Evaluate for parasitized red blood cells.
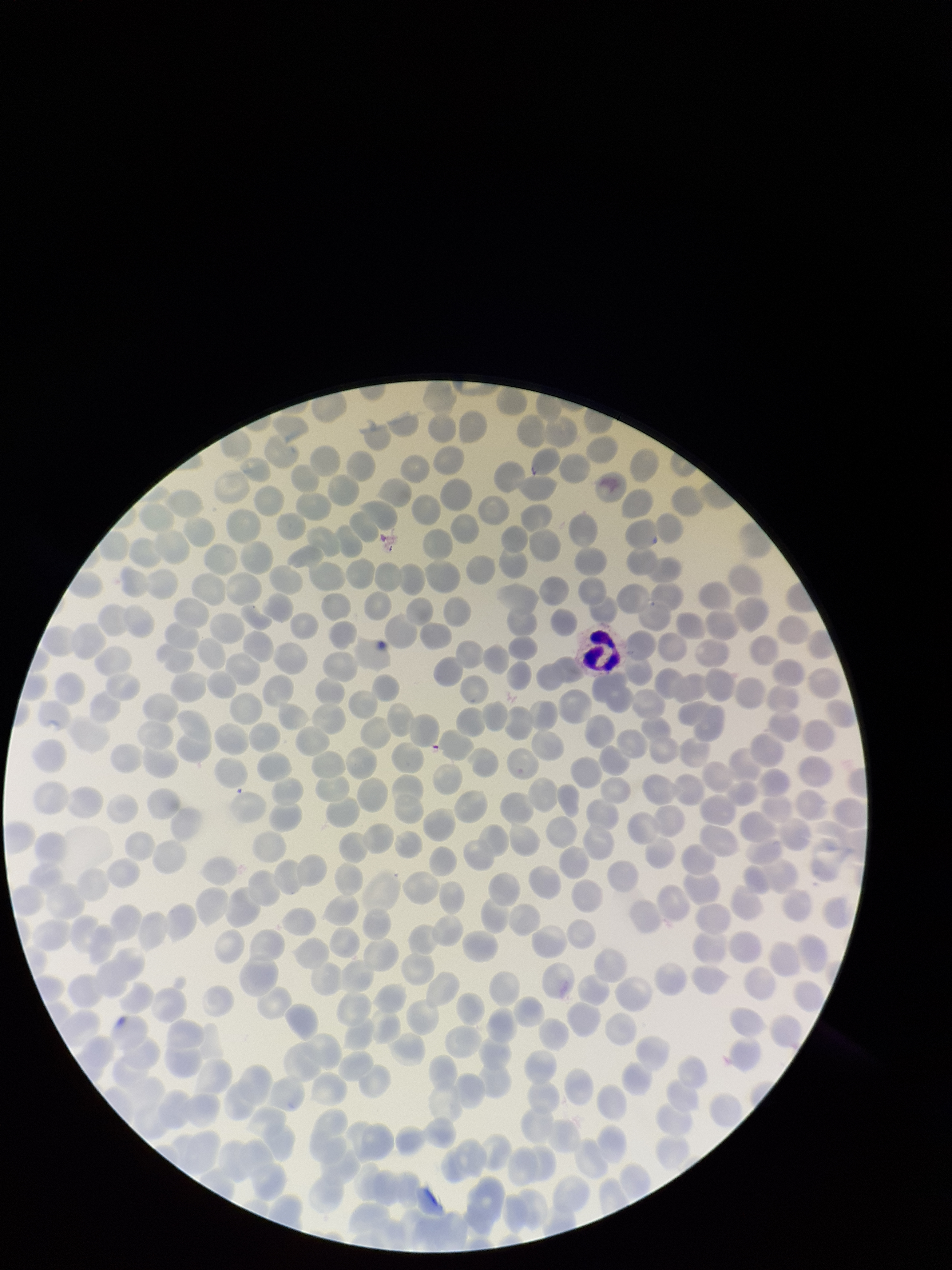

None seen.

parasitized red blood cell count = 0
capture = smartphone photograph through the microscope eyepiece
patient malaria status = infected
red blood cell count = 312
preparation = thin blood smear
stain = Giemsa
species reported for this patient = Plasmodium falciparum
image size = 952×1270 pixels
field of view = one from this slide